Locate every Plasmodium parasite.
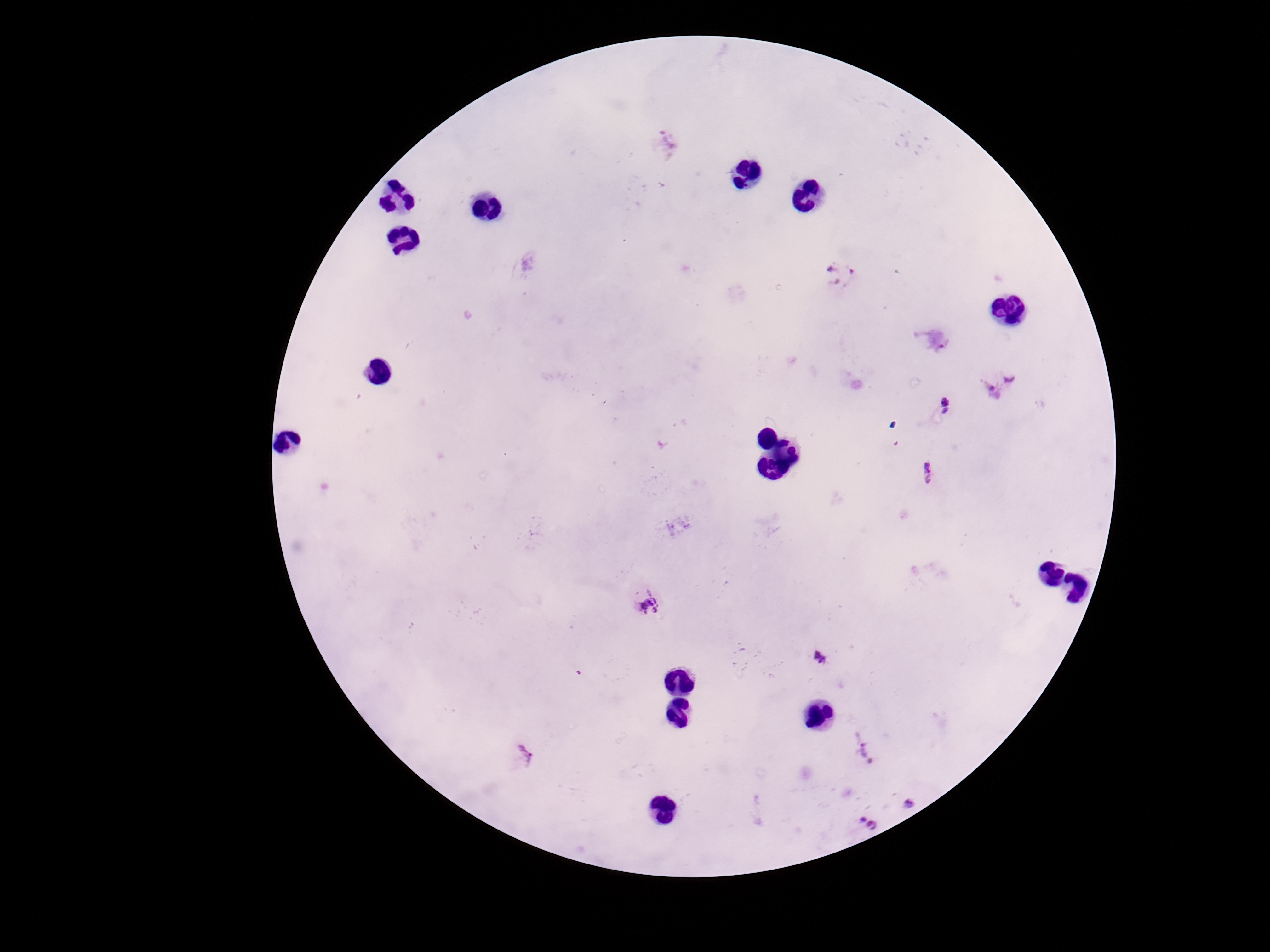
Approximate centers as {x, y} in pixels.
Plasmodium parasites: {670, 141}, {842, 274}, {935, 339}, {1004, 383}, {945, 407}, {928, 473}, {678, 524}, {649, 605}, {818, 659}, {865, 751}, {523, 757}, {909, 803}, {869, 822}.

{
  "patient_malaria_status": "positive",
  "stain": "Giemsa",
  "field_of_view": "one from this slide",
  "preparation": "thick blood film",
  "capture": "smartphone camera through the microscope eyepiece",
  "magnification": "100x",
  "image_size": "1270×952 pixels"
}